Point out each Plasmodium parasite.
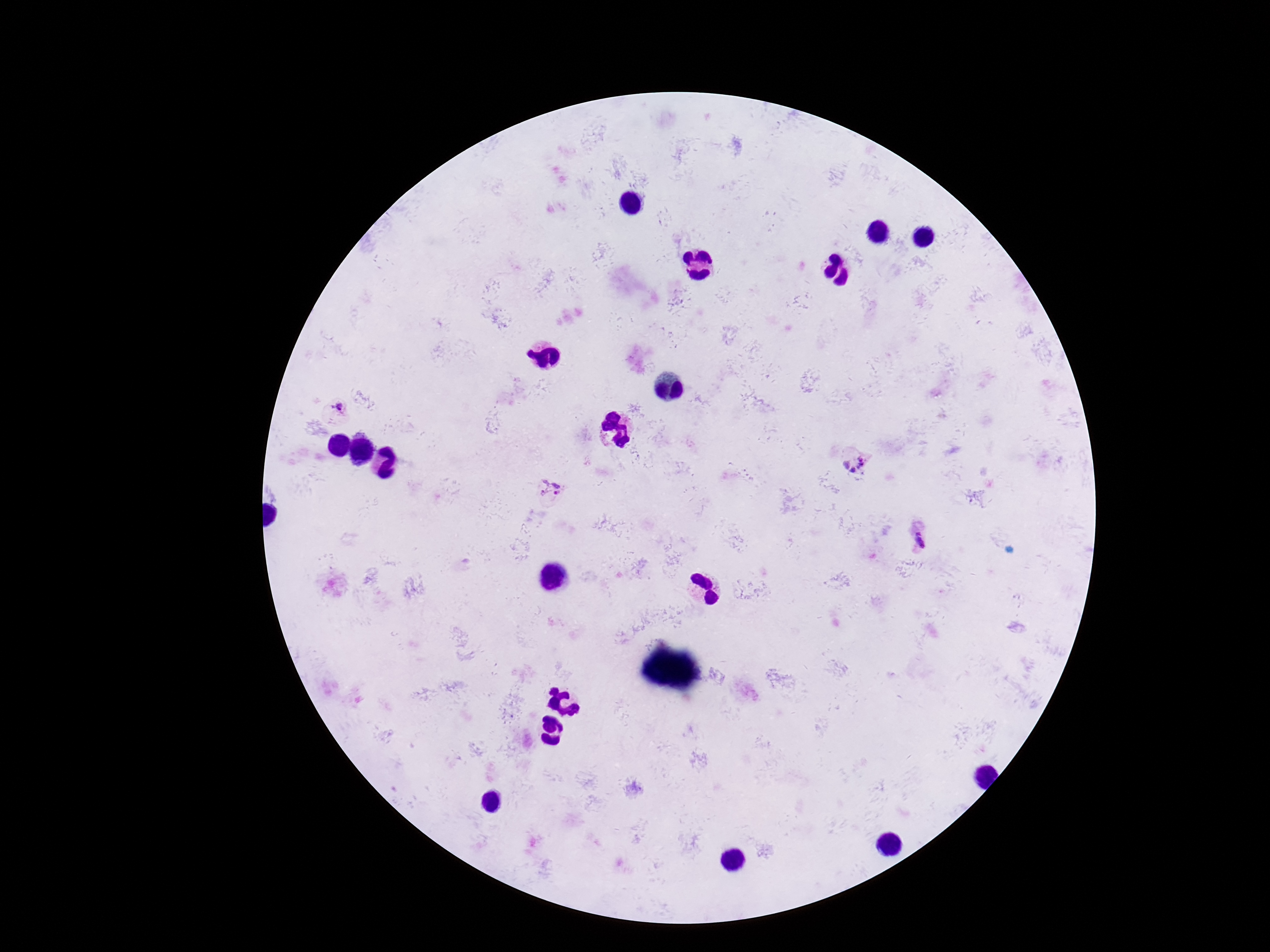

Approximate centers as {x, y} in pixels.
Plasmodium parasites: {336, 409}, {856, 461}, {550, 490}, {919, 541}.

Summary:
  - Patient malaria status: infected
  - Field of view: single
  - Capture: smartphone camera through the microscope eyepiece
  - Image size: 1270×952 pixels
  - Stain: Giemsa
  - Magnification: 100x
  - Preparation: thick blood smear